Locate platelets.
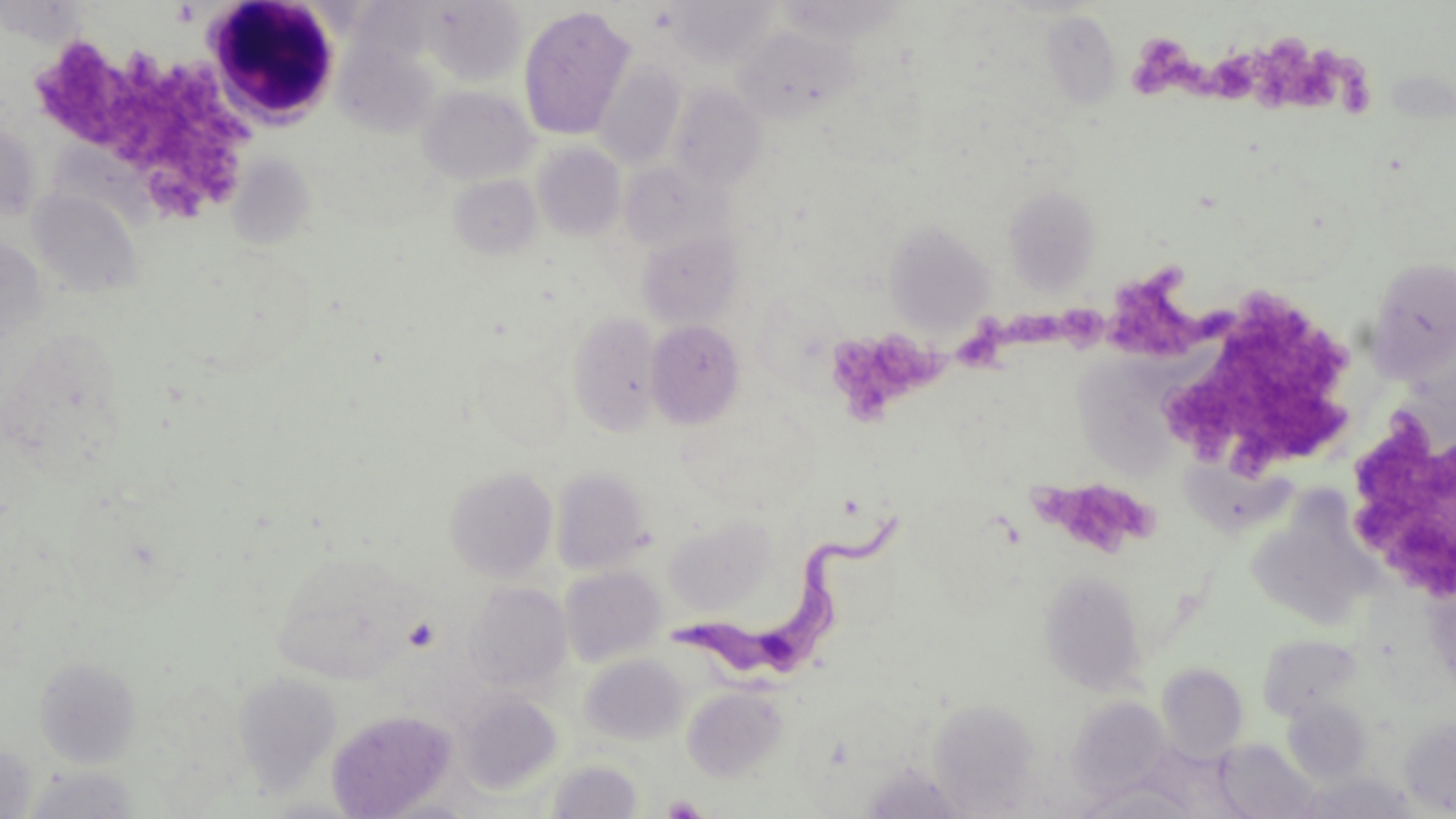
Approximate bounding boxes as [x1, y1, x2, y2] in pixels.
Platelets: [1133, 33, 1220, 109], [1216, 35, 1338, 115], [28, 39, 251, 218], [1337, 71, 1378, 119], [1109, 263, 1237, 364], [1165, 285, 1347, 473], [1051, 301, 1114, 360], [997, 309, 1055, 357], [959, 330, 1005, 371], [828, 334, 957, 430], [1337, 411, 1455, 605], [1030, 475, 1156, 560], [403, 617, 441, 653], [661, 794, 710, 819].

Uninfected red blood cell locations: [775, 0, 908, 43], [423, 1, 528, 86], [666, 1, 780, 70], [518, 6, 636, 141], [1040, 11, 1123, 110], [733, 25, 859, 126], [593, 61, 687, 170], [417, 84, 539, 186], [669, 84, 768, 192], [0, 122, 41, 225], [533, 143, 627, 242], [229, 154, 314, 248], [619, 161, 731, 257], [449, 175, 543, 261], [1003, 185, 1100, 295], [28, 188, 142, 299], [883, 220, 995, 336], [636, 230, 743, 331], [0, 236, 48, 351], [1367, 257, 1456, 380], [569, 311, 664, 436], [646, 319, 745, 429], [1074, 353, 1177, 486], [1168, 458, 1291, 538], [444, 466, 559, 581], [550, 467, 653, 576], [1262, 482, 1385, 629], [664, 514, 776, 615], [272, 550, 416, 685], [559, 565, 666, 667], [1039, 569, 1148, 694], [464, 581, 572, 695], [1256, 634, 1364, 721], [580, 654, 689, 746], [33, 655, 142, 769], [1156, 663, 1249, 761], [233, 672, 342, 795], [682, 686, 790, 782], [457, 692, 563, 795], [930, 694, 1034, 819], [1066, 697, 1172, 797], [1283, 699, 1372, 783], [326, 709, 457, 818], [1399, 715, 1456, 816], [1215, 740, 1322, 818], [0, 741, 37, 818], [545, 760, 643, 818], [857, 764, 975, 819], [21, 767, 144, 818], [1292, 773, 1420, 818], [1072, 780, 1201, 818], [258, 797, 368, 818], [372, 798, 486, 818]. Trypanosoma brucei locations: [673, 507, 904, 690]. White blood cell locations: [201, 1, 345, 130]. Slide-level diagnosis: Trypanosoma brucei. Thin blood film. Image is 1456×819 pixels. Light microscopy. May-Grünwald-Giemsa-stained preparation. 1000x magnification. Single field of view.